Name the cell type shown.
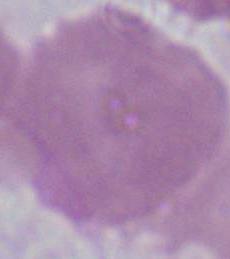

An erythrocyte.

Summary:
  - Modality: photomicrograph
  - Magnification: 1000x